Assess this cell for malaria.
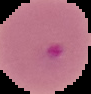

Parasitized.

preparation = thin blood film
image type = cell region segmented out of the field of view; surrounding area masked to black
image size = 91×94 pixels